Locate every blood parasite and identify its species.
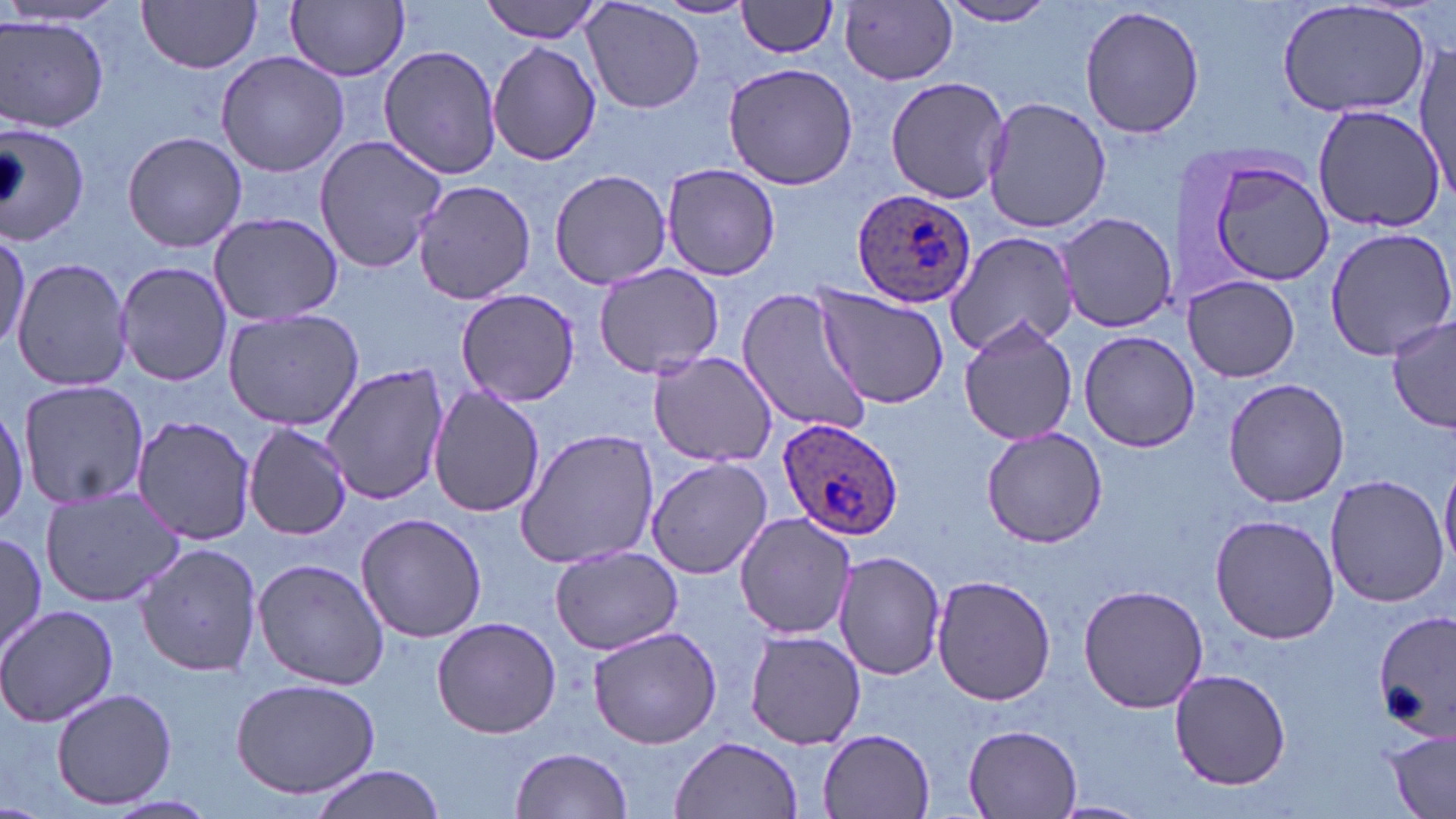
Approximate bounding boxes as (x1,y1)-(x2,y2) corner pairs in pixels.
Plasmodium ovale-infected red blood cells: (851,189)-(978,311), (777,416)-(902,540).
No Plasmodium falciparum, Plasmodium malariae, Plasmodium vivax, Babesia divergens, or Trypanosoma brucei observed.

Uninfected red blood cell locations: (139,0)-(262,73), (288,0)-(408,81), (480,0)-(607,42), (936,0)-(1060,29), (1274,0)-(1434,120), (581,1)-(706,115), (652,1)-(756,21), (736,1)-(841,58), (841,3)-(958,86), (1079,4)-(1206,140), (1,15)-(111,134), (488,42)-(602,166), (379,45)-(503,180), (1413,45)-(1453,196), (215,50)-(349,177), (723,63)-(857,189), (885,77)-(1011,205), (981,96)-(1110,235), (1311,102)-(1445,233), (0,123)-(91,248), (121,131)-(248,253), (314,133)-(447,274), (1194,150)-(1336,290), (659,162)-(781,280), (549,169)-(670,288), (411,178)-(536,306), (208,212)-(344,325), (1056,213)-(1176,334), (1325,229)-(1456,360), (944,231)-(1078,357), (0,232)-(29,352), (11,257)-(133,392), (115,261)-(232,388), (592,264)-(724,379), (1185,273)-(1300,382), (813,284)-(951,409), (736,286)-(873,436), (455,288)-(582,406), (221,308)-(366,430), (958,316)-(1077,445), (1387,316)-(1455,435), (1078,331)-(1199,453), (647,352)-(778,466), (322,361)-(448,505), (1223,378)-(1350,508), (18,380)-(151,510), (428,387)-(545,518), (132,414)-(257,544), (242,423)-(352,541), (982,425)-(1107,549), (513,426)-(660,571), (645,457)-(773,578), (1440,464)-(1456,572), (1326,475)-(1450,609), (40,483)-(190,607), (355,511)-(487,645), (733,511)-(856,639), (1210,514)-(1339,645), (0,533)-(49,662), (135,540)-(263,679), (549,544)-(682,656), (835,552)-(947,680), (251,558)-(390,690), (932,575)-(1057,705), (1077,584)-(1209,714), (1,603)-(119,728), (1373,610)-(1455,740), (431,615)-(562,739), (587,624)-(725,750), (742,631)-(869,749), (1171,669)-(1293,788), (230,676)-(382,799), (51,686)-(178,810), (962,722)-(1085,817), (816,728)-(938,819), (1382,730)-(1456,815), (670,736)-(803,818), (509,747)-(634,818), (308,765)-(446,819), (97,795)-(221,819), (1048,799)-(1148,818). Slide-level diagnosis: Plasmodium ovale. Image is 1456×819 pixels. Optical microscopy. May-Grünwald-Giemsa-stained preparation. Thin blood film. One field of a larger specimen. Captured at 1000x magnification.